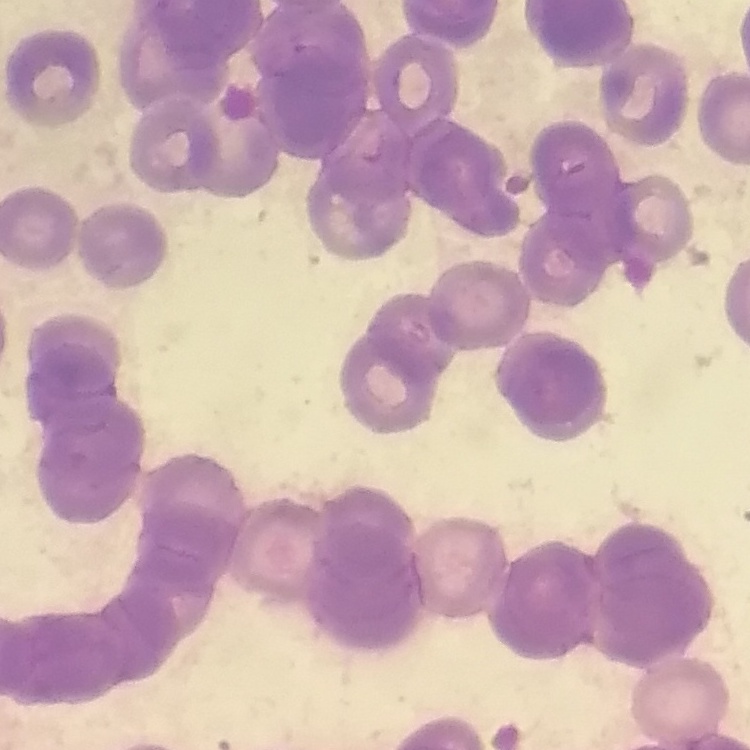

{
  "erythrocyte_morphology": "rouleaux formation",
  "stain": "Field's or Giemsa",
  "image_type": "one tile cut from a larger photomicrograph",
  "preparation": "thin peripheral smear"
}